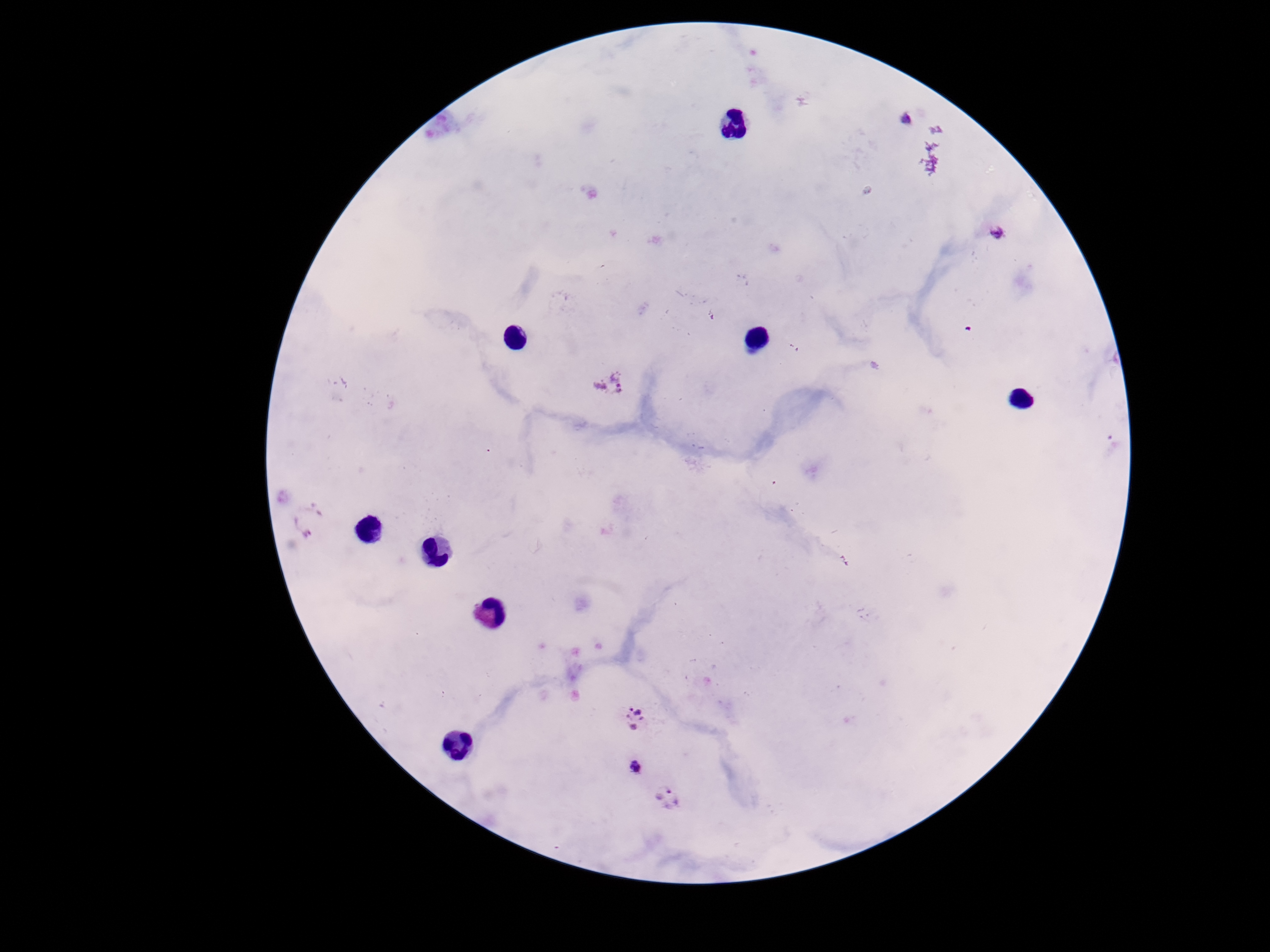 Approximate centers as {x, y} in pixels. Plasmodium parasite locations: {904, 121}, {997, 235}, {614, 383}, {312, 521}, {638, 716}, {637, 768}, {669, 802}. Giemsa-stained preparation. Smartphone photograph taken through the microscope eyepiece. Image is 1270×952 pixels. Single field of view. 100x magnification. Thick peripheral-blood smear. Patient malaria status: infected.